Point out Plasmodium parasites and leukocytes.
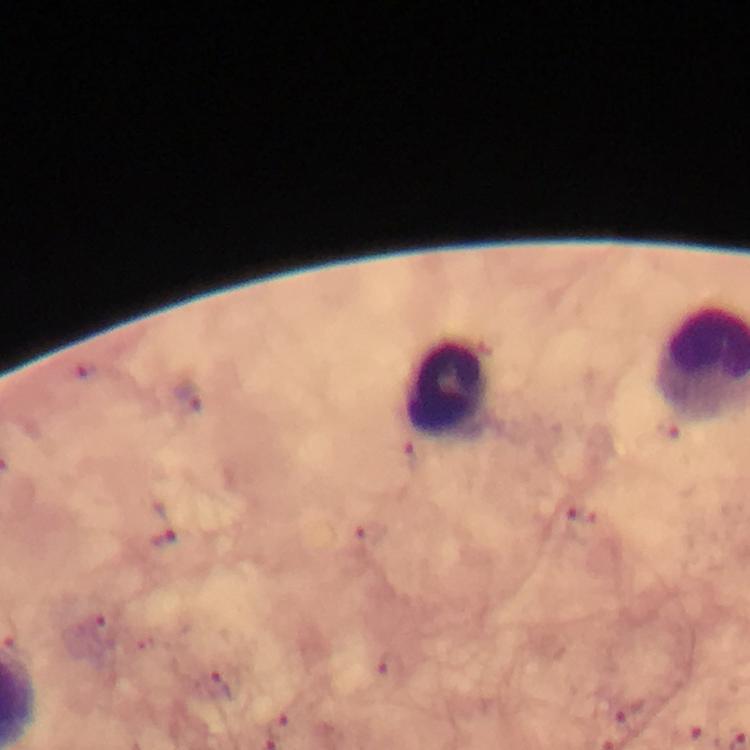
Approximate centers as [x, y] in pixels.
Plasmodium parasites: [84, 373], [188, 396], [667, 430], [411, 454], [568, 508], [370, 535], [164, 539], [103, 634], [213, 685], [279, 725].
Leukocytes: [450, 385].

From a malaria diagnostic workup. Image is 750×750 pixels. Photographed with a smartphone mounted on the microscope. Giemsa-stained preparation. Immersion oil applied. At 100x magnification. Thick blood smear. A crop from one field of view.